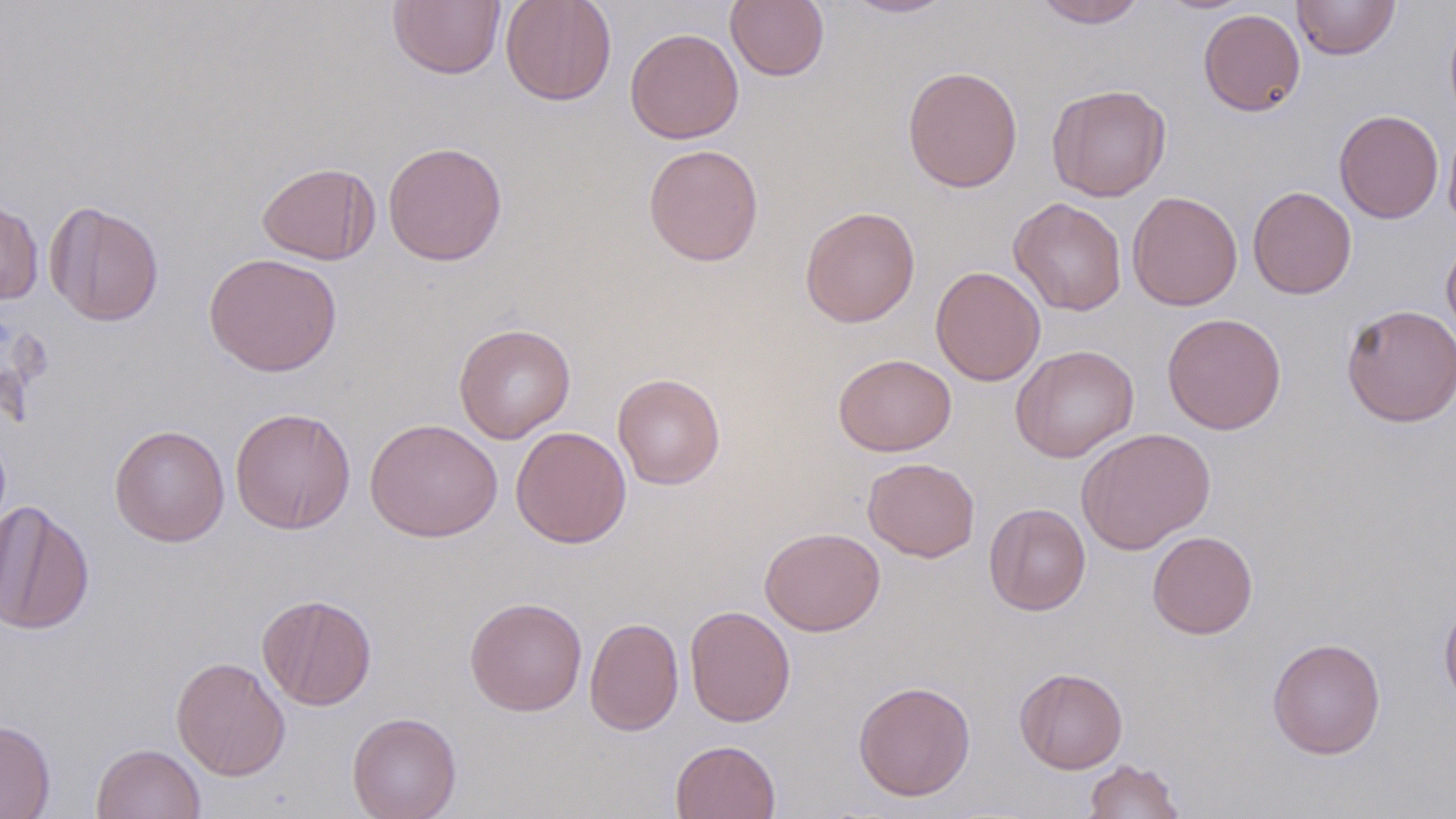 Approximate bounding boxes as (x1, y1, x2, y2) in pixels. Uninfected red blood cell locations: (388, 0, 505, 79), (500, 0, 617, 106), (725, 0, 829, 82), (840, 0, 956, 18), (1034, 0, 1148, 28), (1291, 0, 1399, 60), (1198, 8, 1306, 116), (1444, 9, 1456, 128), (624, 27, 744, 144), (902, 66, 1023, 193), (1047, 83, 1171, 201), (1334, 109, 1444, 223), (1443, 122, 1456, 235), (383, 141, 508, 266), (643, 143, 764, 267), (256, 161, 379, 265), (1247, 186, 1357, 299), (1126, 190, 1242, 311), (0, 196, 44, 305), (1009, 197, 1127, 315), (44, 200, 164, 327), (800, 206, 920, 327), (1441, 237, 1456, 345), (203, 252, 343, 377), (930, 266, 1045, 386), (1341, 303, 1456, 427), (1162, 313, 1287, 435), (453, 323, 576, 443), (1010, 344, 1139, 462), (833, 353, 957, 457), (612, 373, 725, 489), (230, 407, 356, 534), (365, 418, 503, 542), (109, 424, 230, 546), (511, 426, 632, 548), (1076, 427, 1216, 555), (862, 457, 980, 562), (0, 499, 95, 636), (983, 503, 1091, 615), (760, 527, 885, 635), (1147, 530, 1258, 639), (257, 593, 377, 711), (1439, 594, 1456, 712), (464, 596, 588, 716), (684, 605, 796, 727), (584, 616, 684, 736), (1267, 637, 1386, 760), (170, 656, 291, 781), (1014, 667, 1128, 774), (853, 680, 976, 801), (347, 711, 462, 819), (0, 719, 56, 818), (670, 739, 781, 819), (91, 743, 207, 819), (1082, 759, 1185, 818). Slide-level diagnosis: no evidence of blood parasites. Light microscopy. 1000x magnification. Single field of view. May-Grünwald-Giemsa stain. Image is 1456×819 pixels. Thin blood smear.